Give the extent of all Plasmodium ovale-infected red blood cells.
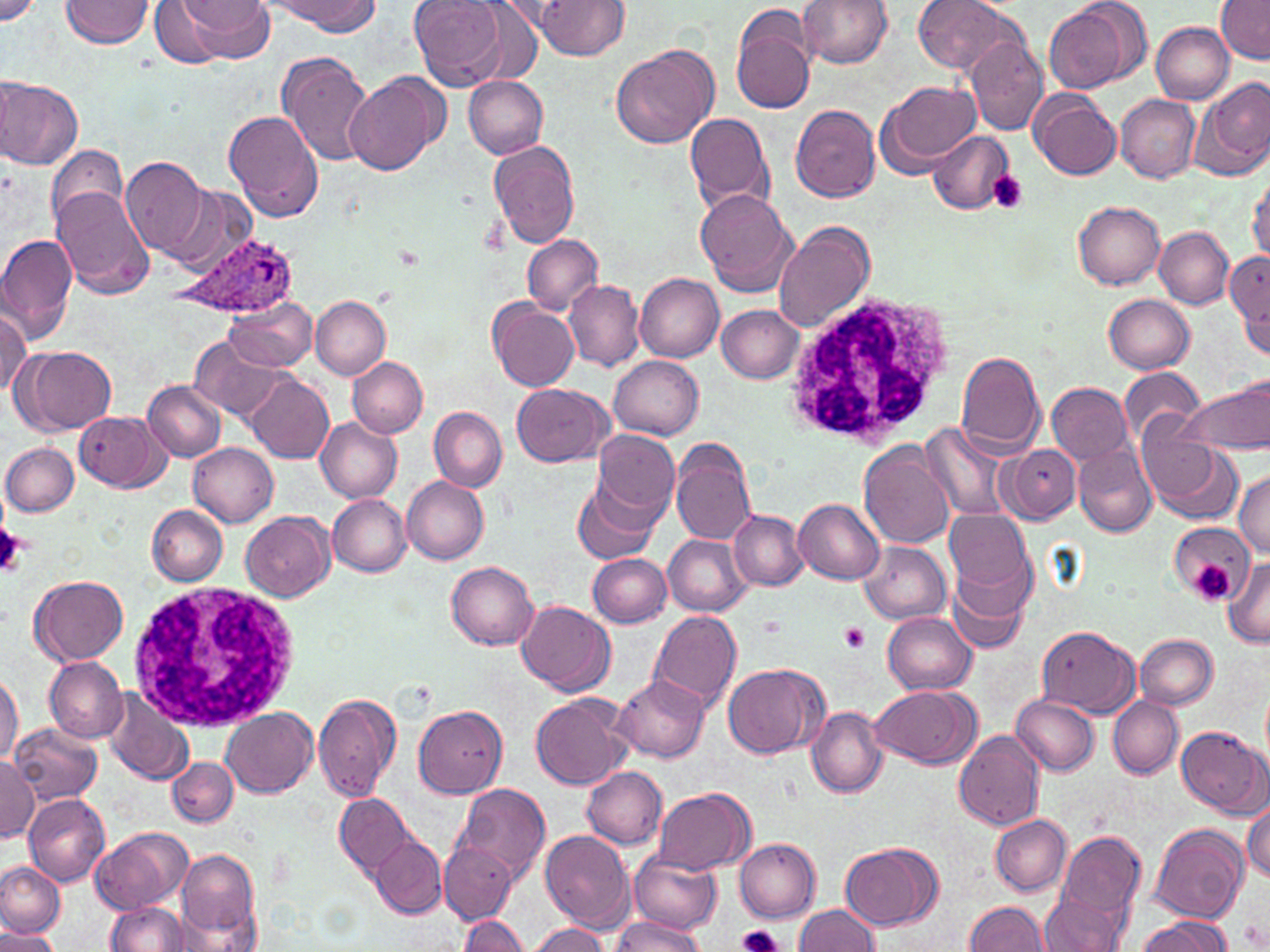
Approximate bounding boxes as (x1,y1)-(x2,y2) corner pairs in pixels.
Plasmodium ovale-infected red blood cells: (170,230)-(299,318).

slide-level diagnosis = Plasmodium ovale
magnification = 1000x
white blood cell locations = approximate bounding boxes as (x1,y1)-(x2,y2) corner pairs in pixels: (785,292)-(958,451), (126,580)-(303,733)
uninfected red blood cell locations = approximate bounding boxes as (x1,y1)-(x2,y2) corner pairs in pixels: (0,0)-(41,27), (61,0)-(154,47), (266,0)-(381,34), (409,0)-(507,90), (536,0)-(629,58), (798,0)-(892,67), (912,0)-(1020,75), (1043,1)-(1147,94), (146,2)-(238,67), (180,2)-(277,61), (1215,2)-(1269,63), (730,3)-(819,116), (1152,22)-(1235,103), (964,37)-(1048,135), (611,43)-(720,149), (276,52)-(375,166), (344,73)-(447,177), (462,74)-(547,158), (0,75)-(82,170), (1194,77)-(1270,182), (878,80)-(981,170), (1030,90)-(1121,180), (1114,94)-(1200,183), (789,104)-(880,202), (225,110)-(324,224), (685,111)-(776,214), (926,132)-(1015,212), (489,139)-(580,249), (45,146)-(132,232), (120,157)-(209,259), (1247,172)-(1270,263), (51,184)-(158,298), (163,186)-(258,277), (696,190)-(798,297), (1072,201)-(1165,289), (773,220)-(876,333), (1154,226)-(1235,309), (0,233)-(79,347), (522,234)-(603,316), (1228,249)-(1270,349), (634,273)-(724,362), (564,279)-(644,371), (1103,293)-(1195,372), (311,296)-(390,379), (224,298)-(317,373), (488,300)-(579,391), (0,304)-(31,399), (717,305)-(804,384), (188,339)-(290,424), (15,345)-(116,434), (954,350)-(1045,454), (610,356)-(705,440), (348,357)-(428,437), (1119,368)-(1205,446), (243,374)-(333,463), (1178,377)-(1270,457), (143,379)-(225,462), (1047,382)-(1134,466), (513,383)-(611,466), (429,407)-(507,493), (74,411)-(170,492), (315,417)-(403,502), (922,423)-(1019,521), (592,429)-(680,524), (0,431)-(140,511), (1138,433)-(1240,523), (670,439)-(756,544), (1,442)-(77,516), (188,442)-(277,526), (858,442)-(956,550), (1073,443)-(1158,537), (1003,446)-(1082,525), (1233,470)-(1270,557), (403,476)-(490,564), (572,478)-(660,565), (328,495)-(412,576), (793,498)-(885,585), (147,505)-(227,585), (945,508)-(1035,598), (730,510)-(807,590), (241,511)-(335,602), (1169,523)-(1250,606), (664,534)-(751,616), (860,541)-(952,624), (946,545)-(1035,654), (589,553)-(671,628), (1224,556)-(1270,645), (446,562)-(539,650), (30,575)-(127,665), (517,600)-(614,695), (649,611)-(742,713), (882,611)-(977,695), (1037,625)-(1141,718), (1135,634)-(1217,709), (44,656)-(127,743), (724,663)-(822,758), (0,669)-(23,768), (613,674)-(710,764), (868,684)-(981,767), (103,690)-(196,789), (530,693)-(629,791), (312,694)-(401,804), (1012,695)-(1101,776), (1109,697)-(1183,778), (414,705)-(507,799), (807,706)-(888,797), (219,707)-(317,798), (8,724)-(102,807), (1177,725)-(1267,816), (953,730)-(1045,832), (0,755)-(38,844), (168,756)-(237,827), (581,764)-(667,850), (452,784)-(551,886), (653,788)-(755,875), (335,792)-(416,877), (23,793)-(110,885), (1245,797)-(1270,885), (990,815)-(1071,897), (1150,823)-(1249,926), (92,827)-(193,913), (1052,829)-(1147,939), (539,830)-(636,932), (371,836)-(448,918), (734,838)-(821,922), (840,841)-(942,931), (442,843)-(515,922), (177,849)-(261,942), (629,850)-(721,936), (0,861)-(67,939), (1039,893)-(1128,951), (106,900)-(190,952), (964,900)-(1049,951), (794,903)-(882,951), (459,914)-(529,952), (1135,916)-(1233,952), (611,918)-(706,951), (525,924)-(611,952), (0,928)-(58,952)
stain = May-Grünwald-Giemsa
field of view = single
image size = 1270×952 pixels
modality = optical microscopy
preparation = thin blood smear
platelet locations = approximate bounding boxes as (x1,y1)-(x2,y2) corner pairs in pixels: (986,170)-(1029,214), (0,517)-(24,575), (1190,559)-(1238,606), (838,622)-(872,653), (737,923)-(785,952)